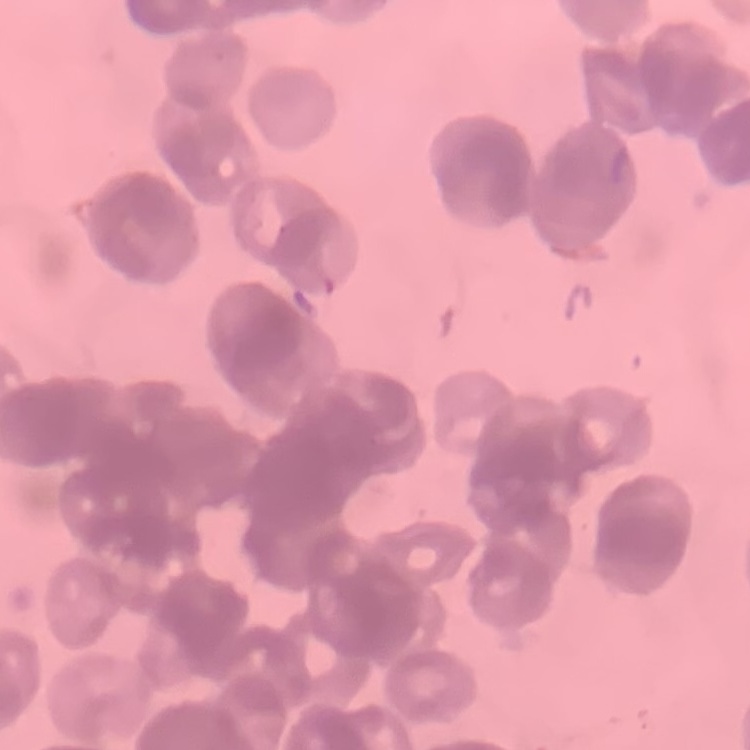
{
  "erythrocyte_morphology": "rouleaux formation",
  "stain": "Field's or Giemsa",
  "preparation": "thin peripheral smear",
  "image_type": "square crop of a larger photomicrograph"
}